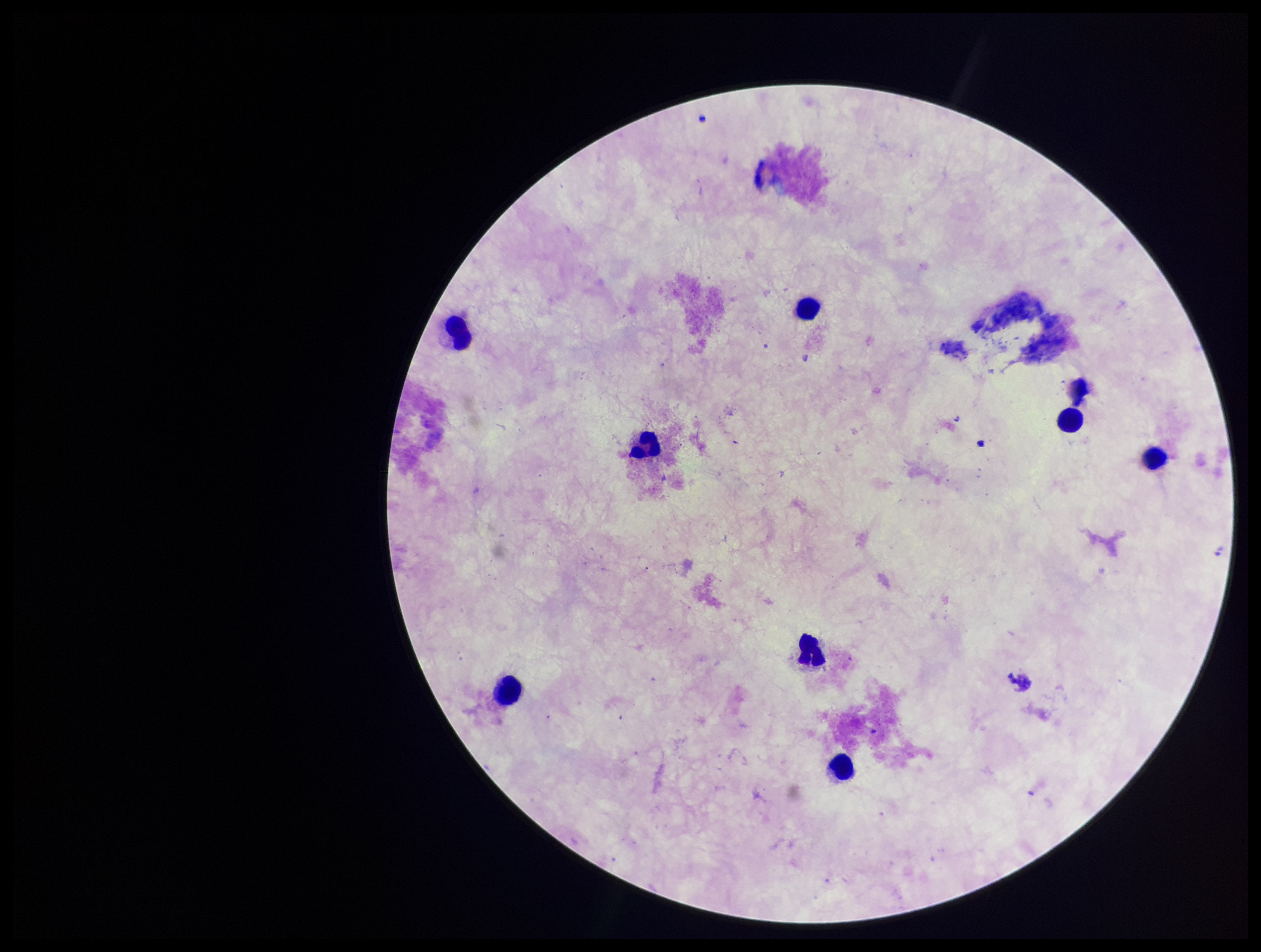 One field from this slide. Stained with Giemsa. Photographed through the microscope eyepiece with a smartphone camera. Plasmodium parasites: none identified. Image is 1261×952 pixels. Leukocyte count: 8. Parasite count: 0. Preparation: thick smear. Patient malaria status: negative.